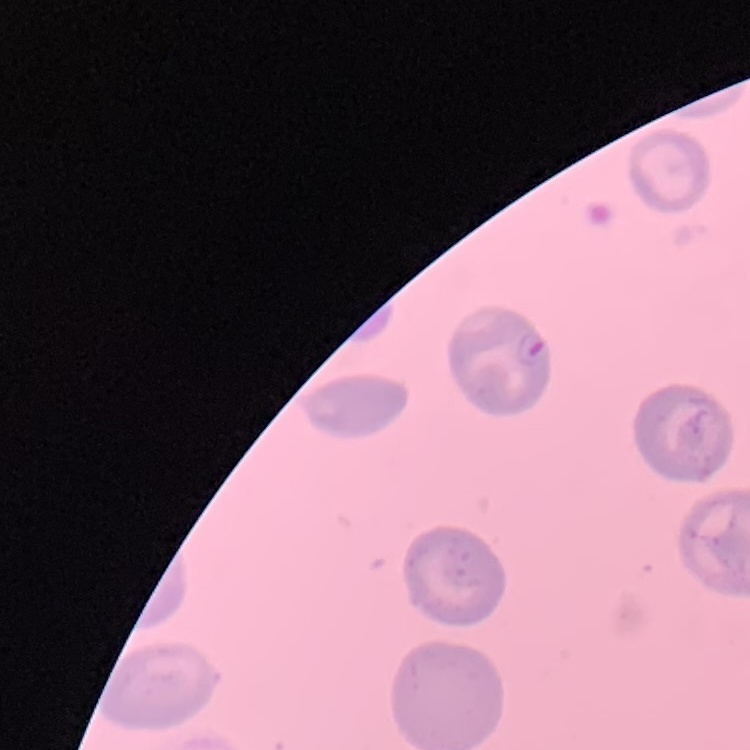

The red blood cells show no rouleaux formation. One tile cut from a larger photomicrograph. Field's or Giemsa stain. Thin peripheral smear.